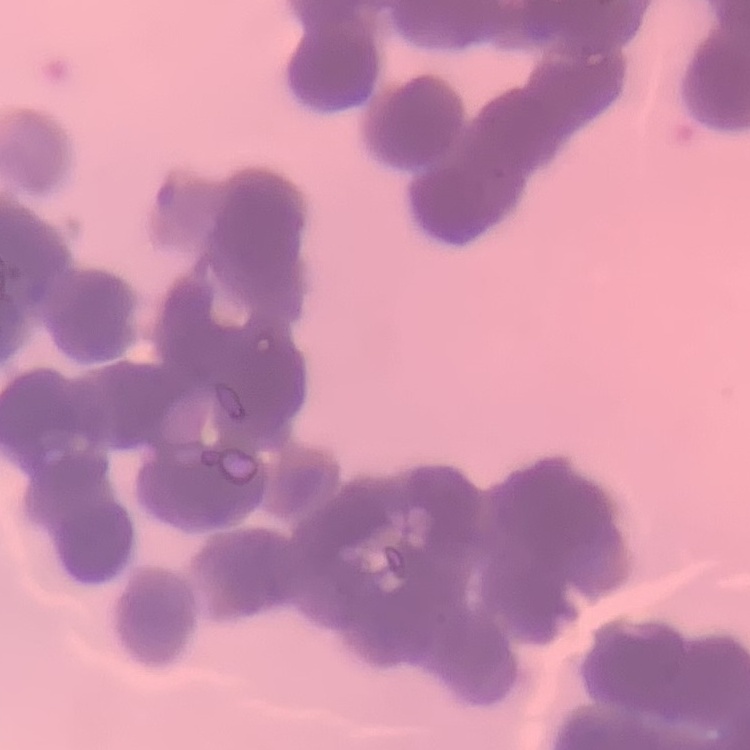

{
  "red_blood_cell_morphology": "rouleaux formation",
  "image_type": "square crop of a larger photomicrograph",
  "preparation": "thin peripheral smear",
  "stain": "Field's or Giemsa"
}